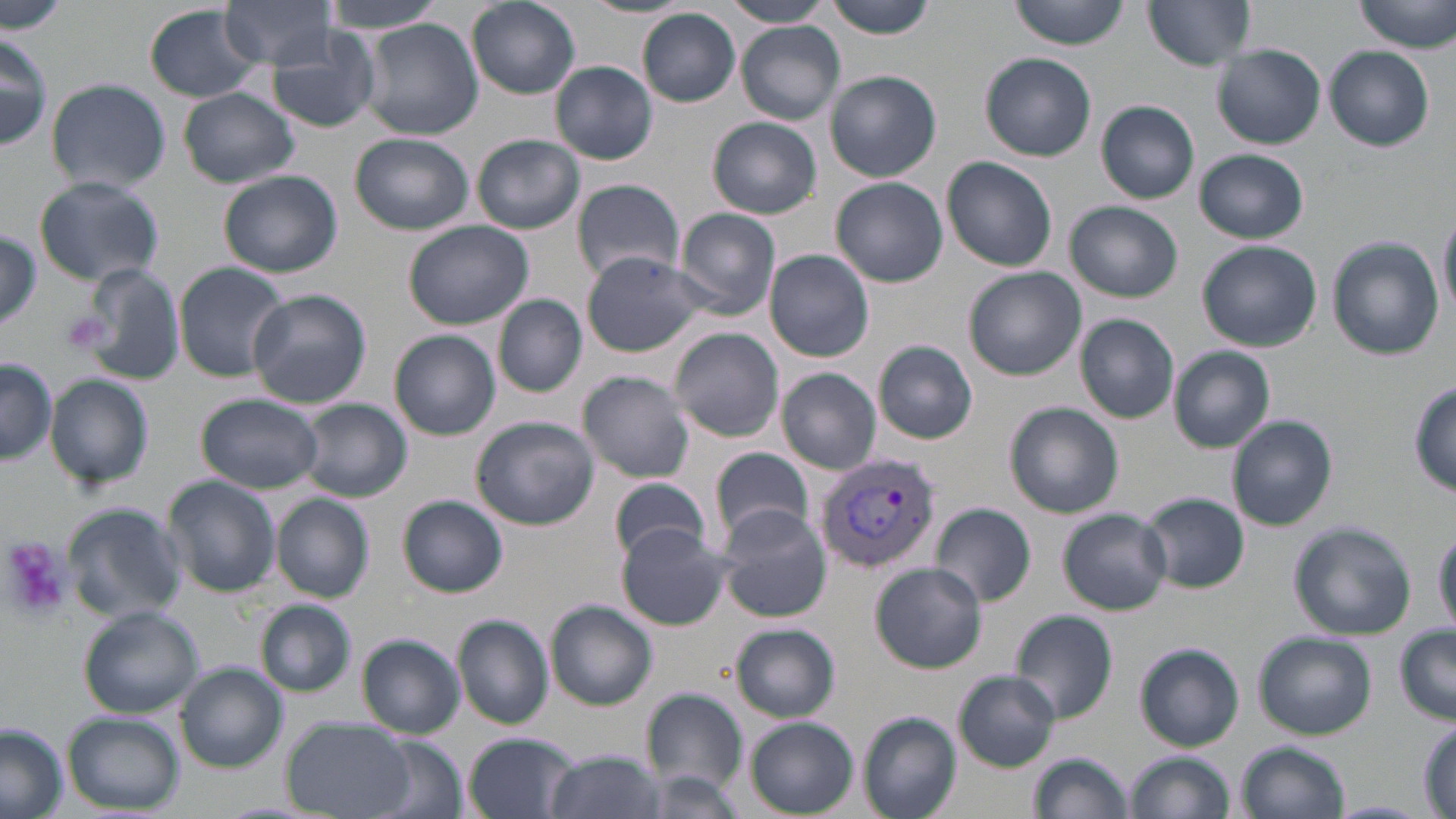
slide-level diagnosis = Plasmodium vivax
stain = May-Grünwald-Giemsa
field of view = single
image size = 1456×819 pixels
preparation = thin blood film
uninfected red blood cell locations = approximate bounding boxes as (x1, y1, x2, y2) in pixels: (0, 0, 71, 35), (220, 0, 341, 70), (319, 0, 450, 34), (466, 0, 580, 100), (584, 0, 691, 20), (824, 0, 942, 39), (1010, 0, 1130, 49), (1143, 0, 1258, 70), (1353, 0, 1456, 53), (724, 1, 834, 28), (145, 4, 262, 102), (637, 8, 741, 107), (362, 19, 482, 140), (735, 21, 844, 124), (0, 29, 51, 155), (267, 31, 382, 133), (1213, 45, 1325, 148), (1326, 45, 1435, 149), (980, 53, 1097, 161), (552, 62, 658, 166), (826, 70, 943, 182), (45, 77, 172, 194), (179, 88, 298, 187), (1097, 101, 1200, 204), (708, 116, 822, 218), (351, 133, 473, 232), (473, 134, 586, 234), (1193, 149, 1308, 243), (941, 157, 1057, 272), (218, 171, 342, 278), (34, 176, 164, 287), (832, 177, 947, 287), (570, 178, 685, 284), (1066, 200, 1182, 303), (672, 207, 783, 318), (1437, 207, 1455, 326), (403, 220, 533, 330), (0, 229, 41, 332), (1327, 237, 1444, 361), (1197, 240, 1322, 352), (765, 249, 875, 362), (581, 251, 710, 358), (173, 263, 291, 382), (74, 264, 186, 387), (964, 267, 1084, 380), (247, 288, 371, 408), (495, 295, 587, 397), (1073, 313, 1179, 424), (668, 327, 785, 442), (390, 330, 500, 440), (874, 341, 978, 444), (1169, 346, 1276, 452), (0, 359, 58, 466), (777, 368, 881, 474), (578, 371, 696, 484), (47, 374, 153, 489), (1411, 379, 1456, 497), (196, 393, 324, 493), (297, 399, 412, 503), (1005, 402, 1125, 518), (471, 415, 598, 530), (1227, 415, 1338, 530), (709, 446, 815, 549), (162, 475, 281, 598), (609, 477, 708, 565), (1141, 492, 1250, 593), (271, 493, 374, 602), (398, 495, 508, 597), (929, 504, 1037, 604), (64, 505, 186, 621), (716, 506, 832, 623), (1059, 508, 1172, 615), (1288, 522, 1417, 639), (616, 524, 731, 630), (1433, 525, 1456, 633), (870, 562, 987, 672), (257, 600, 356, 696), (546, 601, 657, 710), (79, 605, 204, 719), (1010, 611, 1116, 725), (454, 615, 553, 729), (731, 623, 840, 721), (1395, 625, 1456, 724), (1253, 633, 1376, 740), (358, 634, 465, 739), (1135, 643, 1245, 751), (175, 663, 288, 772), (954, 672, 1060, 771), (638, 688, 750, 798), (860, 712, 962, 819), (62, 713, 184, 814), (283, 716, 416, 818), (745, 717, 858, 816), (1411, 717, 1456, 810), (0, 722, 67, 819), (464, 732, 576, 819), (365, 736, 466, 819), (1237, 741, 1350, 819), (541, 750, 664, 819), (1029, 752, 1134, 819), (1127, 752, 1233, 819), (637, 769, 752, 816), (1323, 800, 1435, 818)
magnification = 1000x
modality = light microscopy
platelet locations = approximate bounding boxes as (x1, y1, x2, y2) in pixels: (0, 539, 72, 621)
Plasmodium vivax-infected red blood cell locations = approximate bounding boxes as (x1, y1, x2, y2) in pixels: (815, 452, 940, 575)